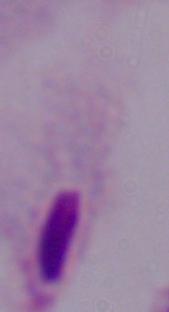

identification = trichomonad
modality = photomicrograph
magnification = 1000x